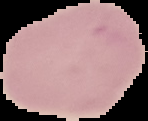
Summary:
  - Image type: segmented cell region on a black background
  - Image size: 148×121 pixels
  - Malaria status: uninfected
  - Preparation: thin blood film